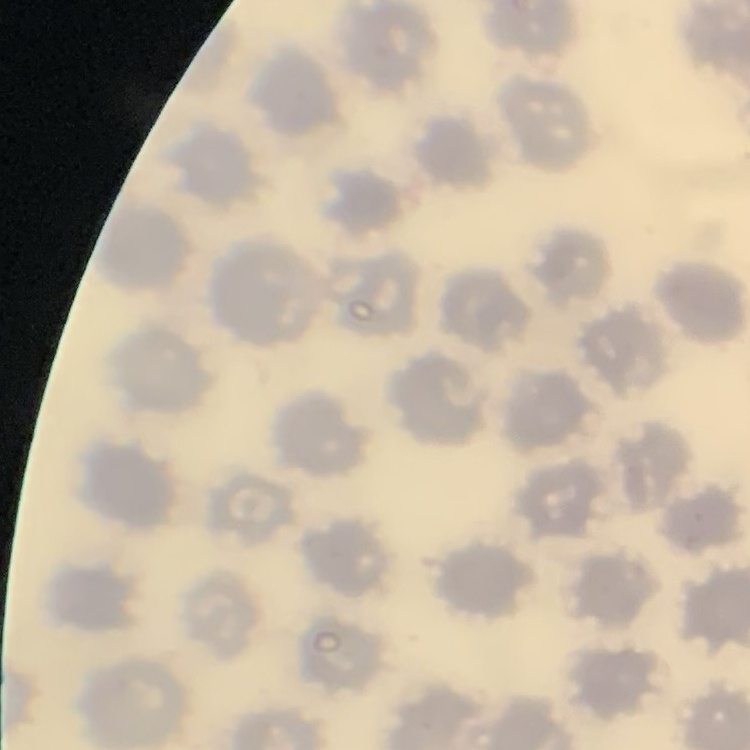

{
  "erythrocyte_morphology": "no rouleaux formation",
  "stain": "Field's or Giemsa",
  "image_type": "square crop of a larger photomicrograph",
  "preparation": "thin blood smear"
}